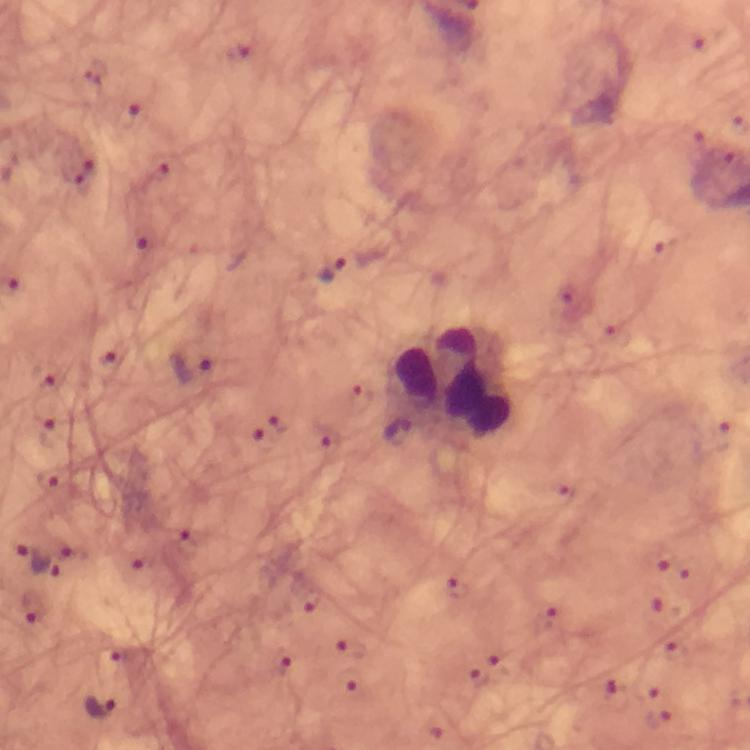
Approximate centers as (x, y) in pixels. Leukocyte locations: (451, 380). Malaria parasite locations: (128, 114), (77, 169), (141, 237), (333, 269), (108, 364), (190, 372), (45, 374), (51, 433), (396, 436), (47, 480), (187, 545), (73, 554), (34, 561), (141, 563), (34, 609), (115, 657), (282, 664), (102, 708). Image is 750×750 pixels. Immersion oil applied. 100x magnification. A crop from one field of view. From a malaria diagnostic workup. Thick blood film. Giemsa-stained preparation. Smartphone photograph taken through a microscope.